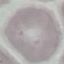

result: no malaria parasites detected
preparation: thin blood smear
stain: Giemsa
capture: smartphone through the microscope eyepiece
image_type: cell patch, automatically extracted from a larger field of view and resized to 64 × 64 pixels